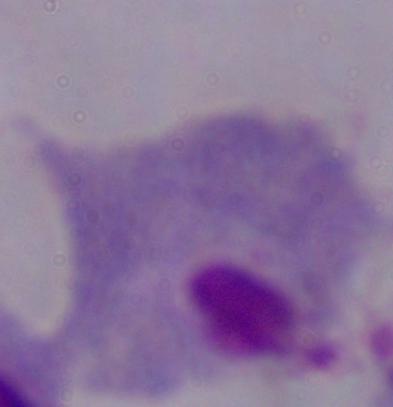

Photomicrograph. 1000x magnification. A trichomonad is shown.